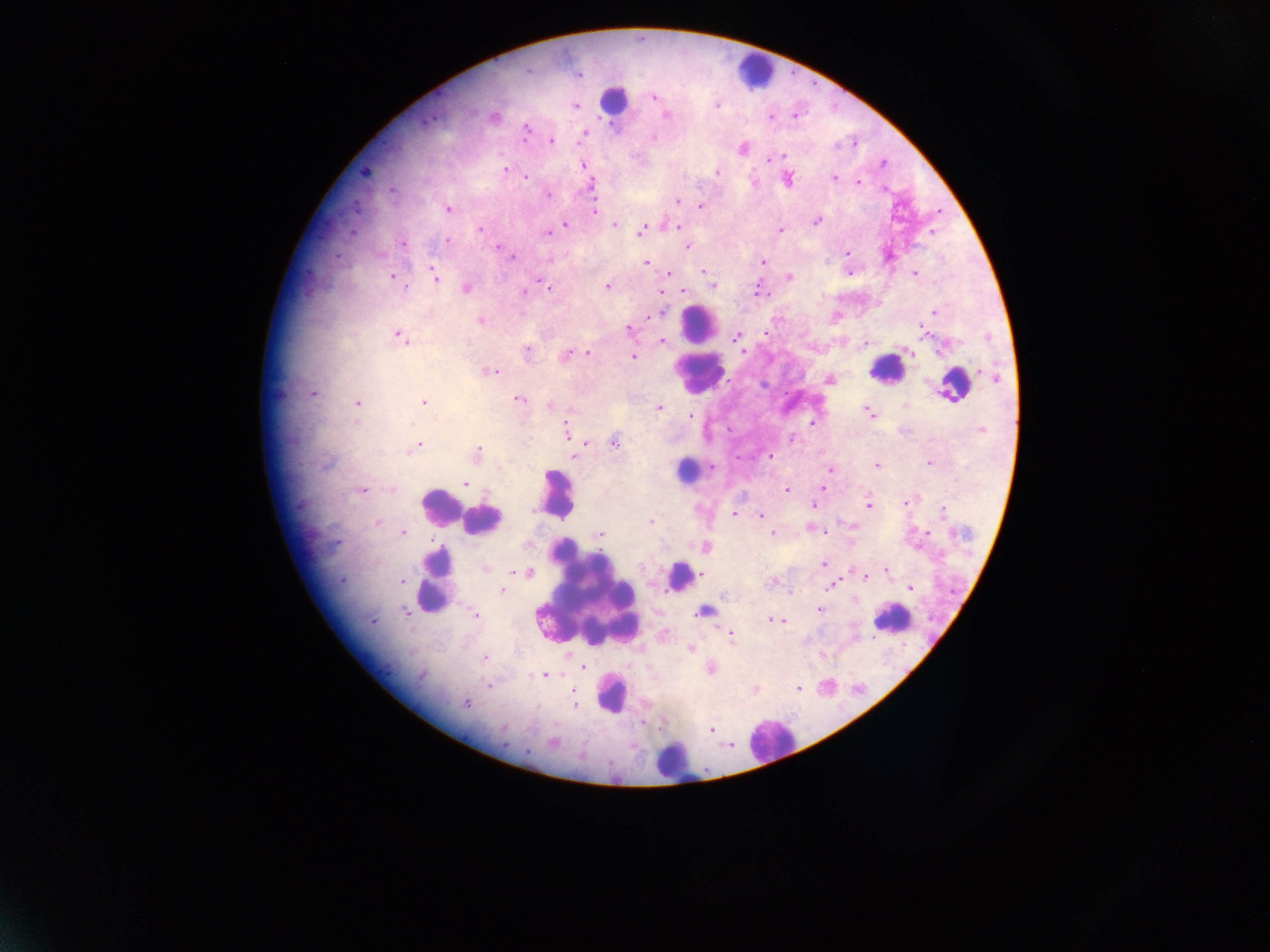
leukocyte locations = approximate centers as {x, y} in pixels: {749, 71}, {618, 102}, {700, 324}, {885, 366}, {695, 375}, {685, 466}, {554, 494}, {440, 506}, {490, 520}, {681, 577}, {433, 582}, {586, 598}, {886, 625}, {612, 698}, {768, 740}, {673, 763}
malaria parasite locations = approximate centers as {x, y} in pixels: {577, 76}, {654, 98}, {575, 106}, {427, 118}, {773, 119}, {526, 131}, {583, 131}, {551, 140}, {742, 146}, {780, 155}, {767, 160}, {582, 163}, {882, 163}, {505, 168}, {718, 172}, {366, 173}, {526, 177}, {833, 178}, {859, 179}, {885, 187}, {548, 195}, {677, 201}, {592, 206}, {700, 206}, {449, 211}, {816, 221}, {661, 224}, {566, 225}, {614, 225}, {680, 227}, {781, 228}, {480, 229}, {642, 231}, {545, 233}, {930, 233}, {447, 241}, {401, 243}, {495, 245}, {686, 246}, {846, 253}, {333, 255}, {512, 258}, {892, 258}, {763, 261}, {431, 263}, {644, 263}, {703, 271}, {670, 273}, {850, 275}, {913, 275}, {391, 276}, {789, 276}, {436, 281}, {711, 281}, {757, 286}, {550, 288}, {607, 288}, {406, 289}, {465, 289}, {661, 291}, {685, 291}, {759, 291}, {526, 292}, {663, 310}, {934, 310}, {648, 317}, {481, 321}, {627, 330}, {922, 331}, {765, 332}, {399, 333}, {735, 336}, {662, 340}, {866, 343}, {527, 350}, {742, 351}, {567, 352}, {589, 353}, {907, 353}, {633, 356}, {494, 370}, {979, 374}, {724, 377}, {994, 377}, {762, 386}, {312, 392}, {278, 393}, {950, 395}, {518, 400}, {358, 403}, {423, 403}, {658, 408}, {869, 416}, {690, 417}, {811, 423}, {566, 426}, {982, 429}, {792, 438}, {614, 440}, {580, 441}, {419, 444}, {479, 451}, {575, 455}, {770, 456}, {928, 463}, {877, 464}, {711, 466}, {324, 467}, {828, 469}, {464, 483}, {822, 487}, {362, 488}, {786, 488}, {868, 503}, {300, 504}, {907, 504}, {814, 505}, {943, 511}, {734, 513}, {762, 517}, {375, 520}, {650, 520}, {848, 526}, {809, 528}, {403, 533}, {600, 535}, {773, 535}, {926, 536}, {334, 544}, {705, 546}, {823, 565}, {485, 568}, {885, 571}, {852, 572}, {521, 573}, {701, 575}, {865, 576}, {341, 581}, {401, 583}, {831, 586}, {909, 589}, {502, 590}, {726, 594}, {819, 609}, {404, 611}, {473, 613}, {694, 615}, {772, 619}, {780, 621}, {372, 623}, {731, 636}, {690, 648}, {484, 658}, {583, 663}, {542, 675}, {421, 677}, {488, 685}, {798, 688}, {756, 690}, {574, 691}, {576, 704}, {466, 705}, {502, 729}, {708, 729}, {554, 742}, {502, 743}, {526, 750}
capture = mobile-phone photograph through a microscope
field of view = single
country = Ghana
image size = 1270×952 pixels
preparation = thick blood film